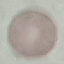
Summary:
  - Malaria status: uninfected
  - Preparation: thin blood film
  - Image type: automatically extracted cell patch, resized to 64 × 64 pixels
  - Capture: smartphone camera at the microscope eyepiece
  - Stain: Giemsa